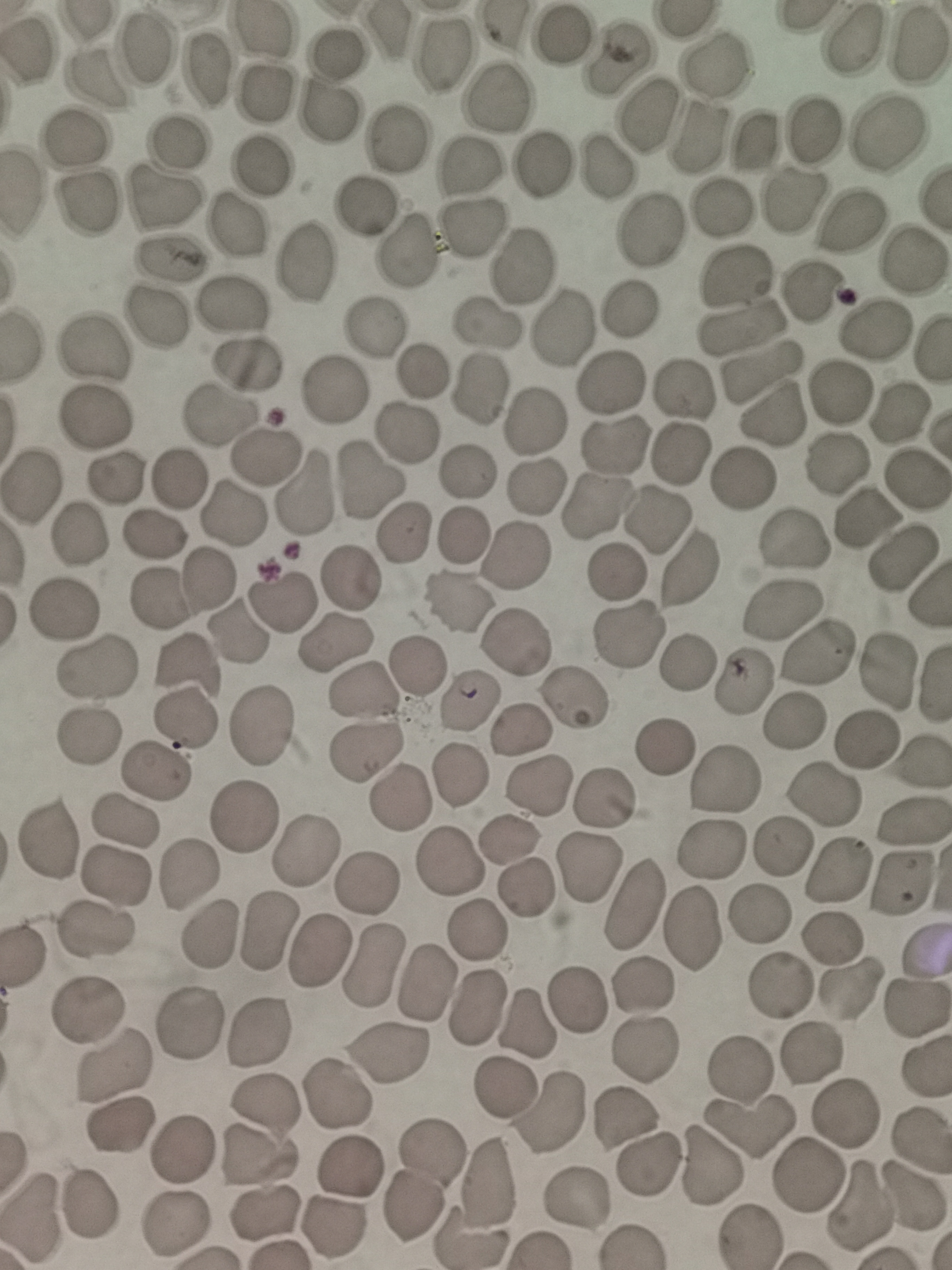

cell locations = approximate centers as {x, y} in pixels: {264, 28}, {562, 37}, {850, 42}, {920, 45}, {147, 50}, {340, 51}, {441, 55}, {617, 58}, {714, 67}, {206, 72}, {95, 80}, {267, 92}, {496, 99}, {328, 115}, {647, 115}, {814, 129}, {889, 135}, {396, 136}, {697, 139}, {77, 140}, {753, 141}, {178, 143}, {261, 165}, {544, 166}, {468, 167}, {609, 169}, {22, 190}, {163, 199}, {796, 199}, {89, 204}, {366, 208}, {722, 209}, {237, 221}, {855, 221}, {473, 227}, {650, 231}, {409, 251}, {173, 259}, {915, 260}, {303, 261}, {522, 268}, {737, 276}, {814, 290}, {229, 305}, {629, 311}, {155, 319}, {485, 323}, {375, 324}, {563, 325}, {742, 330}, {875, 330}, {22, 344}, {91, 349}, {247, 362}, {761, 373}, {421, 374}, {611, 382}, {683, 389}, {475, 390}, {332, 391}, {838, 391}, {900, 416}, {219, 417}, {775, 417}, {96, 418}, {532, 422}, {407, 433}, {615, 443}, {682, 453}, {265, 455}, {839, 462}, {465, 473}, {116, 476}, {742, 479}, {917, 479}, {180, 480}, {366, 482}, {535, 485}, {31, 486}, {301, 493}, {594, 509}, {231, 514}, {866, 519}, {655, 522}, {402, 532}, {79, 533}, {156, 534}, {462, 535}, {794, 540}, {517, 557}, {905, 561}, {691, 569}, {350, 575}, {614, 575}, {208, 580}, {159, 598}, {282, 600}, {459, 601}, {64, 607}, {784, 611}, {236, 632}, {627, 634}, {335, 641}, {514, 642}, {820, 651}, {686, 661}, {187, 664}, {93, 666}, {417, 668}, {884, 670}, {742, 683}, {356, 692}, {571, 697}, {468, 700}, {184, 718}, {793, 723}, {263, 724}, {521, 728}, {89, 734}, {870, 738}, {664, 744}, {363, 753}, {918, 764}, {155, 771}, {459, 777}, {723, 779}, {537, 786}, {821, 796}, {605, 797}, {400, 798}, {242, 815}, {124, 821}, {914, 822}, {47, 838}, {509, 840}, {780, 848}, {713, 850}, {305, 851}, {451, 862}, {589, 869}, {840, 869}, {188, 873}, {115, 875}, {900, 884}, {368, 885}, {525, 889}, {632, 903}, {761, 915}, {694, 929}, {96, 930}, {266, 930}, {478, 932}, {207, 934}, {833, 936}, {319, 949}, {926, 955}, {373, 968}, {425, 984}, {781, 986}, {641, 987}, {852, 990}, {577, 1002}, {474, 1010}, {915, 1011}, {86, 1013}, {528, 1022}, {190, 1023}, {257, 1031}, {647, 1049}, {812, 1054}, {386, 1056}, {112, 1066}, {740, 1069}, {925, 1069}, {507, 1086}, {334, 1094}, {264, 1110}, {846, 1110}, {551, 1114}, {623, 1118}, {749, 1123}, {121, 1124}, {179, 1150}, {259, 1158}, {350, 1165}, {710, 1166}, {646, 1167}, {808, 1173}, {423, 1181}, {489, 1184}, {575, 1198}, {915, 1198}, {91, 1205}, {859, 1207}, {264, 1214}, {30, 1218}, {177, 1227}, {335, 1229}, {746, 1235}, {471, 1241}
field of view = single
stain = Giemsa
preparation = thin smear
capture = smartphone camera at the microscope eyepiece
image size = 952×1270 pixels